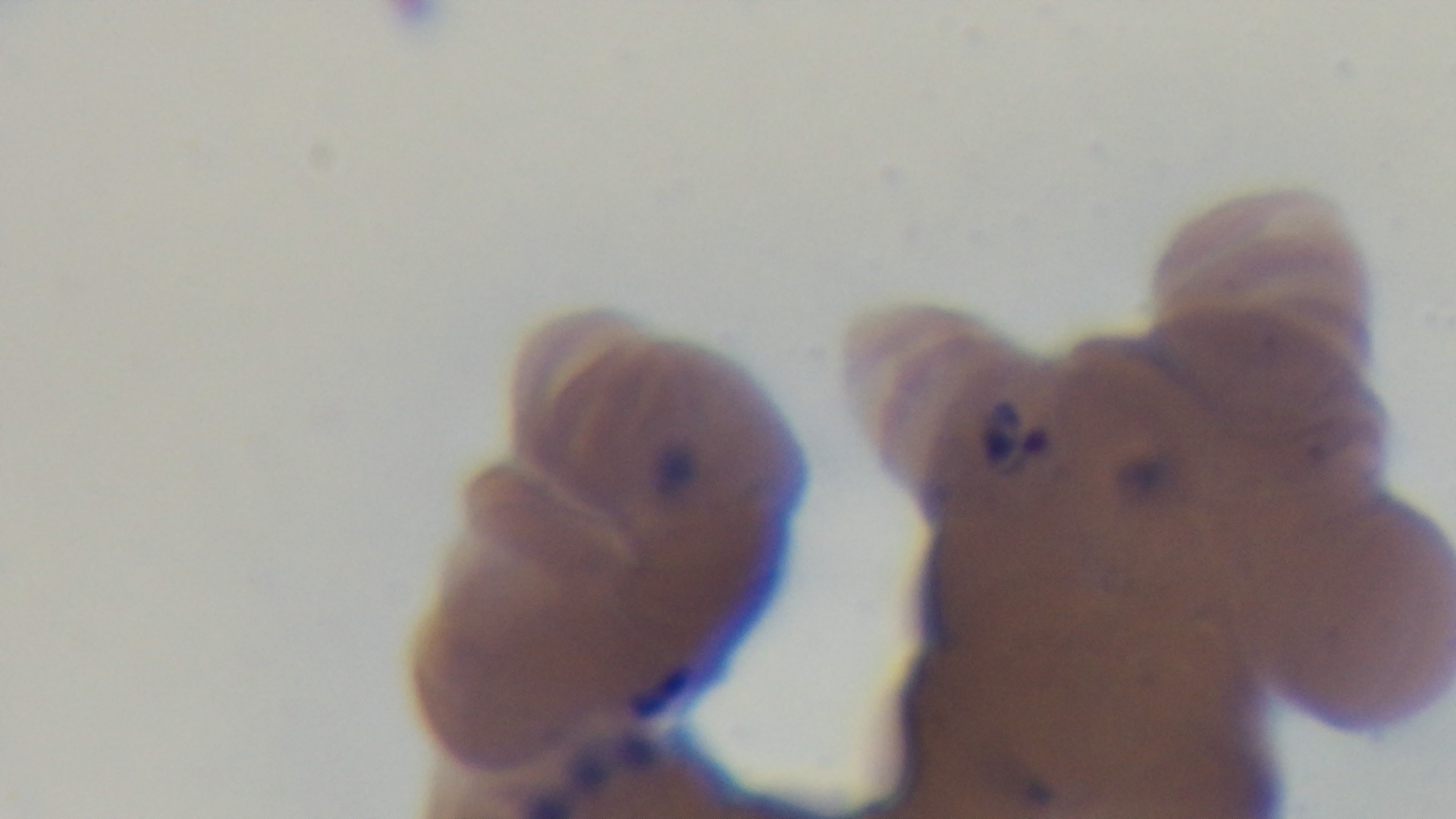
Preparation: thin. Oil-immersion objective, 100x. Single field of view. Malaria status: positive. Mounted 4K digital camera. Photomicrograph. Giemsa stain.